Assess this cell for malaria.
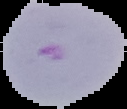
It is parasitized.

From a thin blood film. The area outside the segmented cell region is set to black. Image is 127×109 pixels.